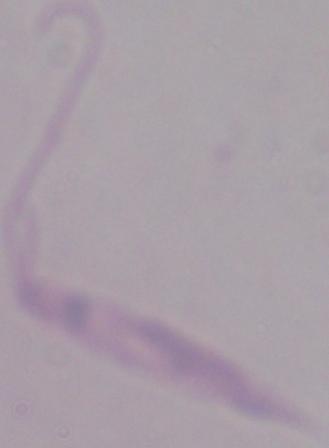
identification = Leishmania
modality = photomicrograph
magnification = 1000x